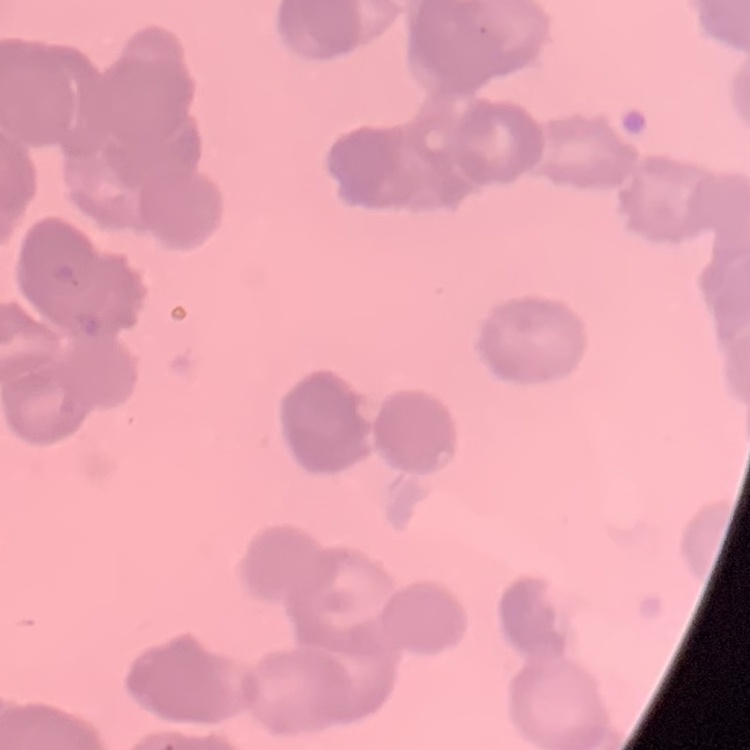
Summary:
  - Red blood cell morphology: rouleaux formation
  - Stain: Field's or Giemsa
  - Image type: one tile cut from a larger photomicrograph
  - Preparation: thin blood film